Locate every malaria parasite.
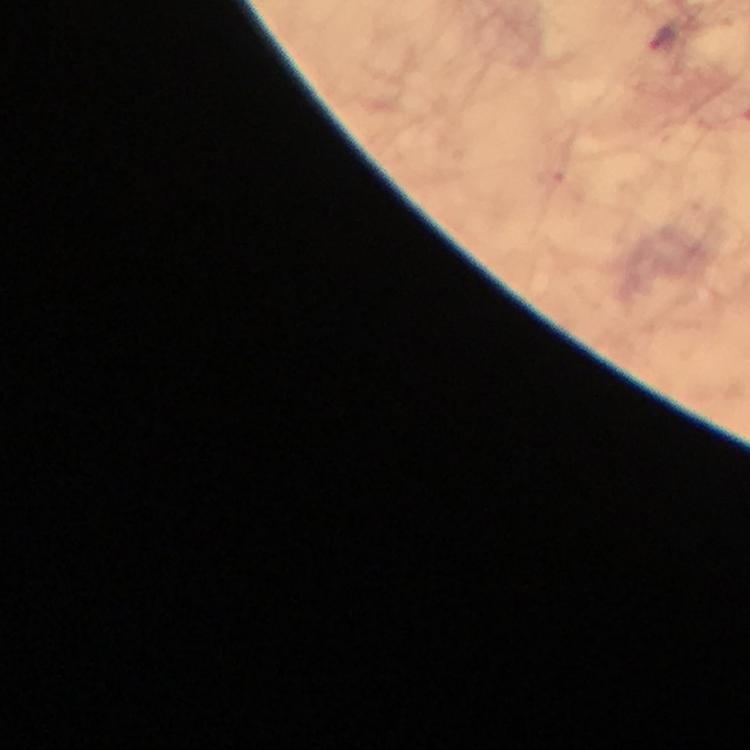

Approximate centers as (x, y) in pixels.
Malaria parasites: (664, 41).

Photographed through the microscope with a smartphone camera. From a diagnostic examination for malaria. Image is 750×750 pixels. Immersion oil applied. 100x magnification. Cropped region of a single field of view. Giemsa-stained preparation. Thick smear.